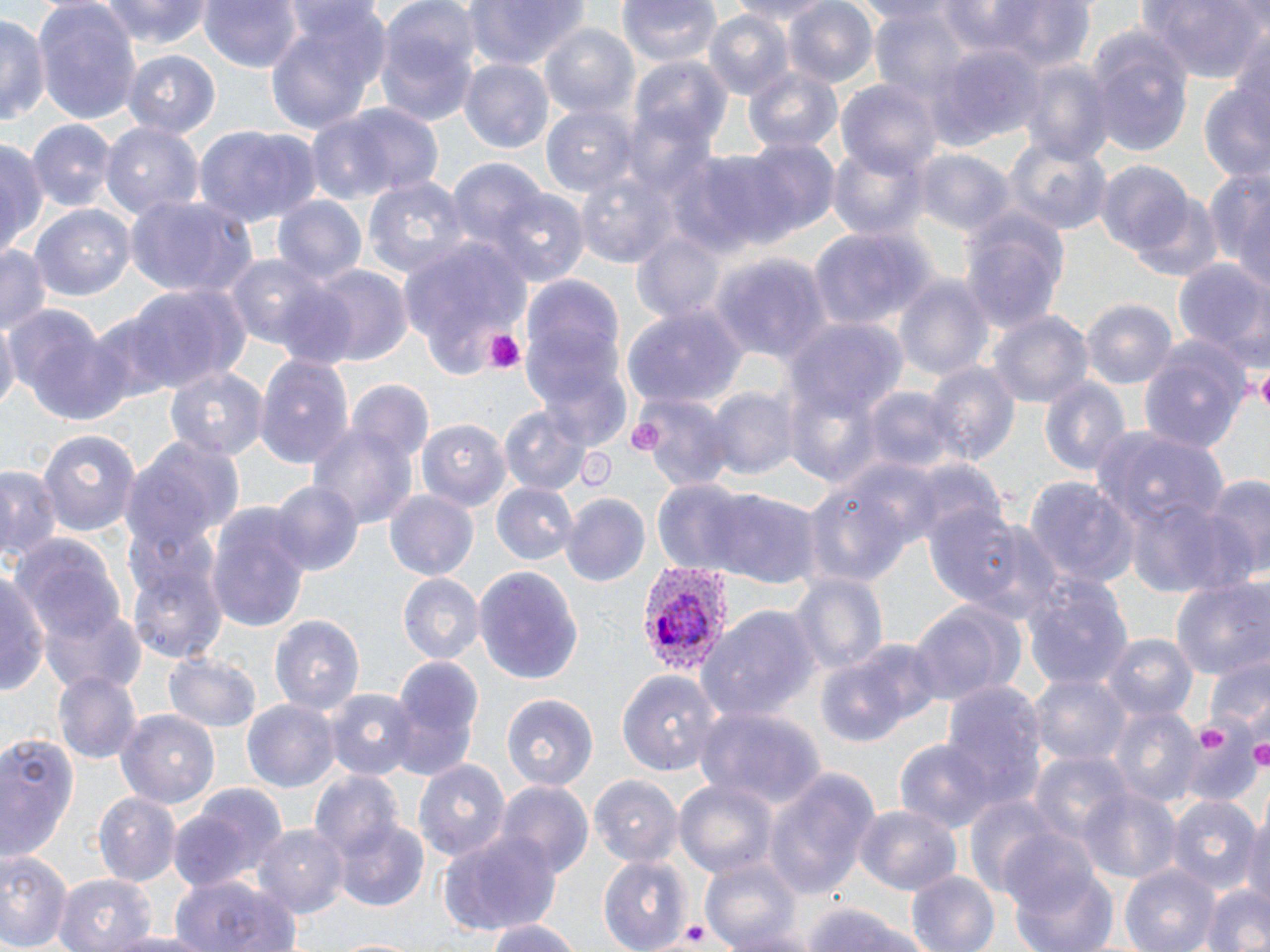

Summary:
  - Coordinate format: approximate bounding boxes as (x1,y1)-(x2,y2) corner pairs in pixels
  - Platelet locations: (481,329)-(527,375), (1255,364)-(1270,409), (1248,732)-(1270,770), (665,918)-(723,949)
  - Uninfected red blood cell locations: (97,0)-(213,49), (199,0)-(306,73), (460,0)-(592,69), (615,0)-(722,67), (728,0)-(838,24), (784,0)-(881,88), (949,0)-(1100,72), (1138,0)-(1269,81), (32,2)-(140,126), (373,4)-(482,129), (261,6)-(388,139), (704,12)-(794,101), (0,13)-(46,130), (539,24)-(641,124), (1084,25)-(1193,154), (929,41)-(1042,150), (121,50)-(220,138), (628,57)-(732,157), (461,58)-(555,154), (741,60)-(843,159), (1019,60)-(1115,163), (837,78)-(941,180), (1198,88)-(1270,185), (310,100)-(442,204), (543,103)-(638,195), (30,120)-(115,212), (100,121)-(203,228), (194,127)-(317,230), (1001,135)-(1113,238), (0,137)-(45,264), (733,138)-(839,242), (828,144)-(929,241), (914,150)-(1014,240), (661,151)-(780,258), (446,158)-(552,261), (1095,161)-(1193,257), (1207,165)-(1270,294), (573,166)-(679,272), (364,176)-(470,284), (376,182)-(501,347), (487,188)-(588,284), (121,192)-(258,296), (1130,193)-(1222,283), (271,194)-(367,292), (30,205)-(134,300), (958,207)-(1070,333), (807,228)-(928,335), (629,234)-(723,327), (402,242)-(530,375), (0,245)-(51,337), (224,252)-(333,354), (710,254)-(833,363), (1171,260)-(1269,354), (306,265)-(412,368), (519,271)-(629,441), (893,273)-(995,388), (122,285)-(241,398), (1083,299)-(1177,391), (6,304)-(116,416), (623,306)-(747,408), (989,311)-(1093,413), (0,317)-(18,415), (787,318)-(907,416), (1139,338)-(1252,451), (253,355)-(355,468), (925,362)-(1019,466), (165,363)-(267,461), (1039,377)-(1131,482), (345,382)-(437,474), (704,385)-(798,480), (863,385)-(959,477), (631,394)-(734,485), (499,406)-(593,495), (420,419)-(510,511), (308,420)-(417,530), (37,426)-(142,535), (1092,426)-(1228,528), (119,436)-(239,563), (0,463)-(63,566), (797,470)-(923,594), (1197,475)-(1270,581), (650,478)-(757,578), (1025,478)-(1137,590), (270,481)-(361,575), (490,481)-(577,564), (712,488)-(820,589), (386,491)-(479,581), (560,493)-(651,586), (1124,496)-(1242,599), (203,499)-(315,636), (945,519)-(1065,624), (12,534)-(126,647), (128,557)-(228,667), (1,566)-(50,696), (475,566)-(583,682), (1018,570)-(1136,698), (792,574)-(885,679), (399,575)-(482,664), (1172,575)-(1270,681), (905,598)-(1024,710), (38,605)-(143,696), (696,606)-(817,726), (269,613)-(366,715), (1104,635)-(1198,724), (815,639)-(933,747), (163,649)-(262,733), (1205,656)-(1270,731), (383,658)-(483,780), (618,669)-(722,777), (1028,671)-(1131,768), (54,672)-(141,764), (942,682)-(1047,812), (325,686)-(417,782), (502,691)-(598,790), (243,700)-(337,791), (694,705)-(821,809), (1109,705)-(1202,807), (117,707)-(219,808), (0,726)-(85,867), (1181,728)-(1258,805), (895,740)-(992,832), (1028,751)-(1131,851), (415,757)-(511,863), (763,769)-(877,900), (308,772)-(406,866), (590,774)-(684,864), (673,775)-(776,878), (495,780)-(593,878), (167,786)-(287,893), (1079,786)-(1182,887), (92,793)-(180,884), (963,795)-(1062,898), (1167,797)-(1260,893), (853,804)-(963,894), (1242,812)-(1270,910), (334,817)-(432,911), (258,825)-(347,916), (438,831)-(562,932), (0,848)-(72,952), (599,851)-(689,950), (701,852)-(805,952), (1119,864)-(1219,952), (1013,865)-(1121,952), (905,869)-(1000,952), (55,872)-(158,952), (169,873)-(301,952), (1198,880)-(1270,952), (799,901)-(934,952), (482,920)-(585,952), (104,930)-(212,952), (331,936)-(427,952)
  - Plasmodium vivax-infected red blood cell locations: (636,558)-(731,677)
  - Slide-level diagnosis: Plasmodium vivax
  - Preparation: thin blood smear
  - Modality: light microscopy
  - Image size: 1270×952 pixels
  - Magnification: 1000x
  - Field of view: one of a larger specimen
  - Stain: May-Grünwald-Giemsa